Locate and identify every blood parasite.
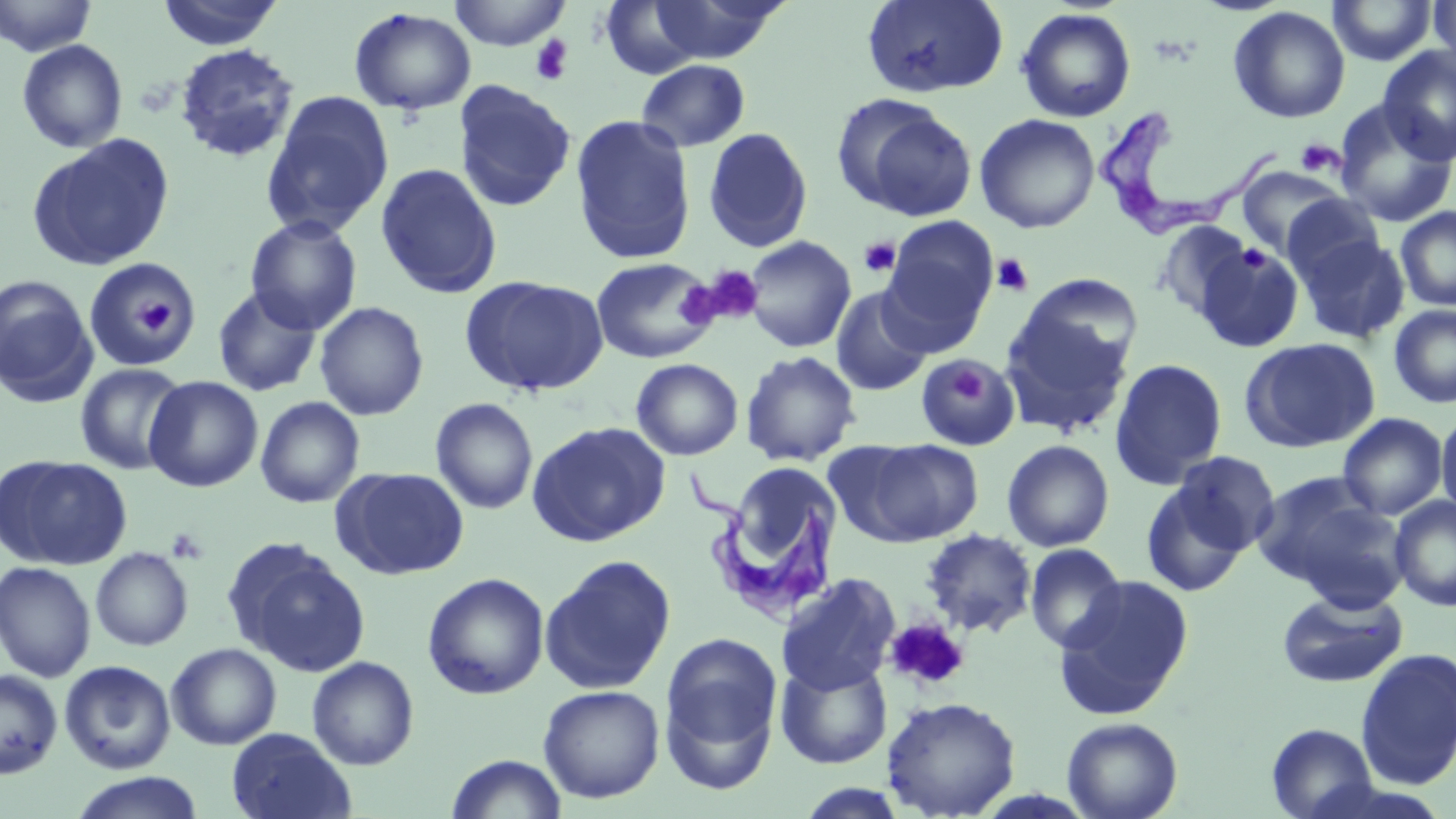
Approximate bounding boxes as (x1, y1, x2, y2) in pixels.
Trypanosoma brucei: (1096, 110, 1284, 240), (686, 462, 845, 620).
No Plasmodium falciparum, Plasmodium ovale, Plasmodium malariae, Plasmodium vivax, or Babesia divergens observed.

slide-level diagnosis = Trypanosoma brucei
platelet locations = approximate bounding boxes as (x1, y1, x2, y2) in pixels: (530, 35, 574, 86), (1295, 138, 1344, 176), (858, 237, 901, 277), (992, 254, 1034, 297), (697, 265, 764, 325), (127, 287, 183, 342), (946, 363, 987, 406), (166, 527, 209, 565), (884, 618, 969, 691)
stain = May-Grünwald-Giemsa
preparation = thin blood film
field of view = single
image size = 1456×819 pixels
modality = light microscopy
uninfected red blood cell locations = approximate bounding boxes as (x1, y1, x2, y2) in pixels: (0, 0, 98, 57), (156, 0, 286, 50), (447, 0, 572, 50), (644, 0, 789, 65), (861, 0, 1009, 98), (1328, 0, 1437, 66), (1428, 0, 1455, 77), (599, 2, 710, 79), (1228, 6, 1350, 123), (1016, 7, 1136, 123), (349, 8, 476, 115), (16, 39, 128, 153), (174, 43, 300, 164), (1377, 45, 1456, 165), (636, 59, 751, 152), (453, 80, 576, 212), (260, 90, 395, 238), (833, 95, 979, 221), (1334, 102, 1456, 227), (974, 114, 1100, 234), (570, 115, 696, 264), (590, 126, 802, 261), (703, 127, 813, 252), (26, 134, 176, 272), (375, 163, 502, 299), (1237, 165, 1347, 257), (1281, 193, 1385, 285), (1395, 207, 1456, 311), (245, 215, 362, 334), (880, 216, 999, 349), (1153, 220, 1255, 321), (1296, 233, 1410, 344), (742, 236, 856, 353), (1193, 241, 1304, 353), (83, 256, 203, 371), (590, 257, 721, 364), (0, 274, 98, 407), (460, 274, 610, 397), (1018, 274, 1144, 377), (211, 285, 323, 398), (831, 287, 933, 397), (313, 301, 429, 421), (999, 303, 1135, 438), (1389, 305, 1456, 408), (1240, 338, 1380, 453), (740, 350, 861, 466), (916, 354, 1018, 451), (631, 358, 743, 460), (1109, 358, 1228, 490), (74, 363, 189, 475), (143, 375, 263, 492), (255, 397, 365, 508), (430, 397, 538, 514), (1436, 408, 1456, 522), (1337, 412, 1449, 520), (527, 421, 670, 547), (853, 438, 984, 546), (1002, 440, 1115, 552), (1169, 450, 1281, 558), (1, 455, 133, 570), (332, 467, 470, 579), (736, 469, 835, 563), (1254, 473, 1402, 602), (1140, 476, 1252, 597), (1390, 496, 1456, 612), (920, 528, 1037, 637), (222, 538, 371, 677), (1024, 544, 1127, 654), (90, 547, 193, 651), (539, 555, 676, 694), (0, 560, 96, 681), (422, 572, 549, 700), (776, 573, 901, 695), (1053, 576, 1195, 719), (1276, 589, 1408, 688), (659, 630, 783, 782), (166, 643, 282, 750), (1355, 648, 1456, 790), (775, 655, 893, 769), (306, 656, 419, 770), (60, 660, 176, 774), (0, 668, 63, 779), (539, 684, 665, 803), (881, 695, 1021, 818), (1062, 716, 1183, 819), (1266, 722, 1378, 819), (225, 727, 357, 819), (446, 754, 567, 818), (70, 772, 204, 819)
magnification = 1000x